Classify this cell by malaria status.
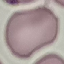
It is uninfected.

Acquired by smartphone through the microscope eyepiece. Automatically extracted cell patch, resized to 64 × 64 pixels. Giemsa stain. Thin blood smear.